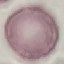
{
  "result": "no malaria parasites detected",
  "capture": "smartphone camera at the microscope eyepiece",
  "preparation": "thin blood film",
  "stain": "Giemsa",
  "image_type": "automatically extracted cell patch, resized to 64 × 64 pixels"
}